Classify this cell by malaria status.
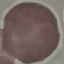

Uninfected.

Summary:
  - Preparation: thin blood smear
  - Image type: automatically extracted cell patch, resized to 64 × 64 pixels
  - Capture: smartphone camera at the microscope eyepiece
  - Stain: Giemsa